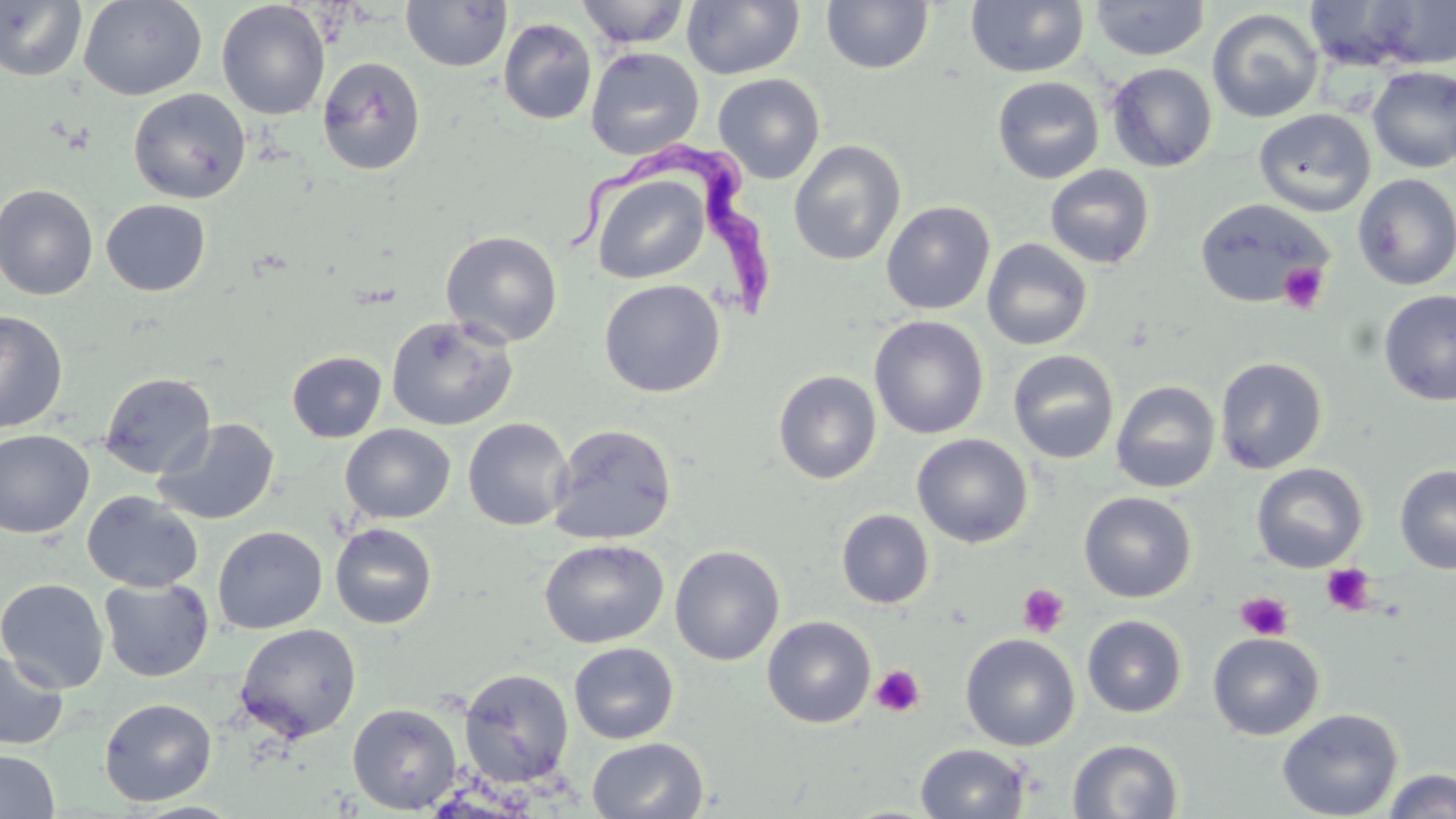

Approximate bounding boxes as named x1/y1/x2/y2 corners in pixels. Uninfected red blood cell locations: (x1=78, y1=0, x2=207, y2=101), (x1=575, y1=0, x2=690, y2=49), (x1=965, y1=0, x2=1089, y2=78), (x1=1368, y1=0, x2=1456, y2=69), (x1=0, y1=1, x2=87, y2=82), (x1=216, y1=1, x2=330, y2=120), (x1=401, y1=1, x2=512, y2=72), (x1=682, y1=1, x2=805, y2=80), (x1=820, y1=1, x2=934, y2=74), (x1=1089, y1=1, x2=1210, y2=61), (x1=1301, y1=1, x2=1435, y2=73), (x1=1207, y1=8, x2=1324, y2=123), (x1=498, y1=18, x2=597, y2=125), (x1=584, y1=46, x2=704, y2=161), (x1=316, y1=56, x2=426, y2=176), (x1=1107, y1=62, x2=1217, y2=172), (x1=1367, y1=65, x2=1456, y2=173), (x1=713, y1=73, x2=825, y2=184), (x1=992, y1=76, x2=1104, y2=184), (x1=128, y1=88, x2=250, y2=203), (x1=1253, y1=108, x2=1375, y2=216), (x1=788, y1=139, x2=906, y2=267), (x1=1045, y1=165, x2=1155, y2=269), (x1=589, y1=172, x2=711, y2=285), (x1=1352, y1=173, x2=1456, y2=290), (x1=0, y1=183, x2=99, y2=301), (x1=1194, y1=198, x2=1333, y2=308), (x1=101, y1=200, x2=211, y2=296), (x1=881, y1=201, x2=996, y2=315), (x1=441, y1=230, x2=563, y2=348), (x1=981, y1=238, x2=1093, y2=351), (x1=599, y1=279, x2=726, y2=397), (x1=1378, y1=289, x2=1456, y2=406), (x1=0, y1=310, x2=68, y2=433), (x1=869, y1=315, x2=989, y2=439), (x1=386, y1=316, x2=519, y2=431), (x1=1007, y1=349, x2=1120, y2=464), (x1=286, y1=351, x2=387, y2=442), (x1=1214, y1=356, x2=1328, y2=474), (x1=773, y1=370, x2=882, y2=484), (x1=99, y1=372, x2=215, y2=478), (x1=1110, y1=380, x2=1221, y2=493), (x1=153, y1=418, x2=280, y2=525), (x1=462, y1=418, x2=574, y2=531), (x1=547, y1=423, x2=678, y2=544), (x1=340, y1=424, x2=455, y2=523), (x1=0, y1=429, x2=95, y2=538), (x1=911, y1=433, x2=1033, y2=548), (x1=1251, y1=462, x2=1368, y2=572), (x1=1394, y1=464, x2=1456, y2=574), (x1=82, y1=490, x2=203, y2=593), (x1=1078, y1=491, x2=1197, y2=603), (x1=836, y1=509, x2=935, y2=608), (x1=330, y1=523, x2=437, y2=629), (x1=212, y1=526, x2=327, y2=634), (x1=539, y1=539, x2=668, y2=649), (x1=669, y1=545, x2=785, y2=666), (x1=0, y1=578, x2=109, y2=694), (x1=99, y1=578, x2=214, y2=682), (x1=1082, y1=614, x2=1187, y2=718), (x1=762, y1=616, x2=876, y2=728), (x1=234, y1=624, x2=362, y2=743), (x1=1207, y1=632, x2=1325, y2=740), (x1=960, y1=633, x2=1080, y2=751), (x1=568, y1=642, x2=679, y2=745), (x1=0, y1=650, x2=68, y2=750), (x1=458, y1=667, x2=574, y2=787), (x1=99, y1=698, x2=217, y2=806), (x1=347, y1=703, x2=462, y2=814), (x1=1277, y1=708, x2=1403, y2=819), (x1=587, y1=737, x2=709, y2=819), (x1=1067, y1=738, x2=1184, y2=819), (x1=915, y1=743, x2=1031, y2=819), (x1=0, y1=749, x2=60, y2=818), (x1=1381, y1=769, x2=1456, y2=819), (x1=126, y1=801, x2=246, y2=818). Platelet locations: (x1=1278, y1=261, x2=1329, y2=314), (x1=1321, y1=563, x2=1376, y2=615), (x1=1017, y1=583, x2=1070, y2=638), (x1=1236, y1=592, x2=1294, y2=640), (x1=870, y1=664, x2=926, y2=718). Trypanosoma brucei locations: (x1=563, y1=140, x2=779, y2=318). Slide-level diagnosis: Trypanosoma brucei. Image is 1456×819 pixels. 1000x magnification. May-Grünwald-Giemsa stain. Single field of view. Thin blood film. Optical microscopy.